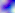
modality = photomicrograph
identification = Toxoplasma gondii
magnification = 400x